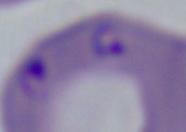

Captured at 1000x magnification. A Babesia parasite is seen. Photomicrograph.